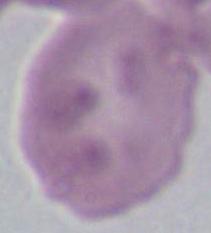
magnification: 1000x
identification: red blood cell
modality: micrograph